Classify this cell by malaria status.
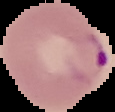
It is parasitized.

Segmented cell region on a black background. Image is 115×112 pixels. From a thin blood film.